Locate every Plasmodium falciparum-infected red blood cell.
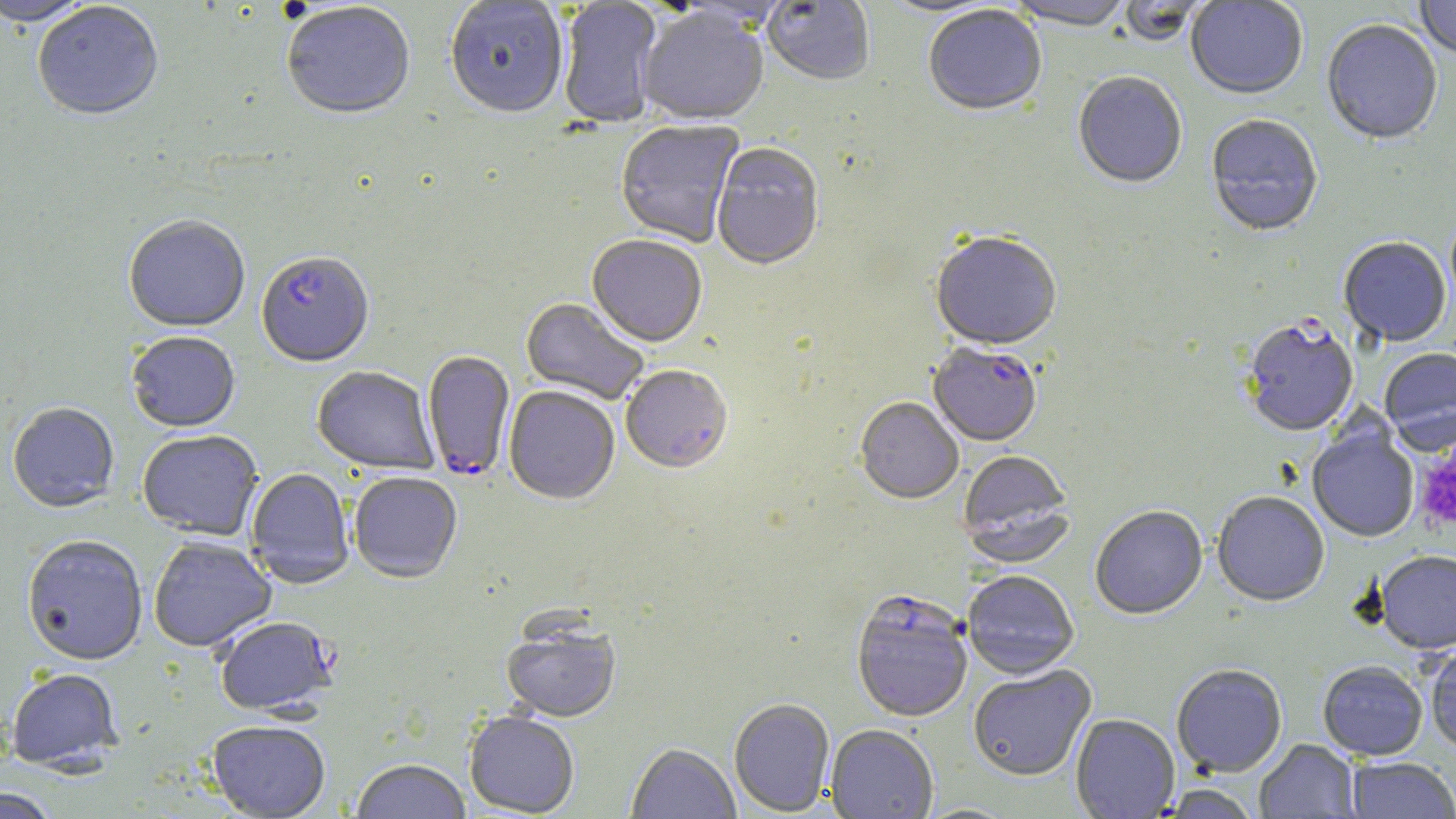

Approximate bounding boxes as [x1, y1, x2, y2] in pixels.
Plasmodium falciparum-infected red blood cells: [257, 254, 374, 369], [1242, 321, 1359, 438], [928, 345, 1042, 449], [422, 351, 515, 482], [851, 592, 973, 724], [214, 617, 338, 718].

Platelet locations: [1414, 449, 1456, 532]. Uninfected red blood cell locations: [762, 0, 875, 88], [877, 0, 1005, 18], [1186, 0, 1308, 101], [1414, 0, 1456, 60], [0, 1, 93, 28], [444, 1, 568, 122], [557, 1, 664, 130], [1007, 1, 1133, 34], [1117, 1, 1210, 48], [33, 3, 163, 124], [281, 4, 415, 123], [923, 6, 1047, 118], [637, 9, 769, 128], [1321, 21, 1442, 147], [1072, 74, 1187, 191], [1205, 115, 1323, 239], [615, 121, 745, 248], [711, 144, 824, 273], [123, 217, 250, 334], [930, 234, 1062, 352], [587, 237, 707, 350], [1339, 239, 1451, 348], [520, 299, 648, 405], [126, 333, 240, 434], [1379, 349, 1456, 454], [312, 367, 440, 475], [621, 367, 733, 477], [503, 387, 620, 506], [855, 399, 963, 506], [7, 403, 120, 514], [1307, 428, 1419, 543], [137, 431, 263, 541], [957, 453, 1075, 567], [246, 469, 354, 590], [349, 473, 462, 584], [1211, 493, 1329, 609], [1090, 507, 1208, 621], [21, 536, 148, 667], [149, 537, 276, 654], [1375, 553, 1456, 656], [962, 571, 1079, 681], [501, 622, 620, 723], [1425, 646, 1456, 754], [1318, 663, 1427, 761], [968, 666, 1096, 782], [1171, 666, 1287, 779], [6, 668, 123, 773], [729, 699, 835, 816], [464, 712, 579, 817], [1071, 715, 1179, 818], [207, 722, 331, 818], [826, 726, 938, 819], [1254, 740, 1360, 818], [627, 744, 740, 818], [1346, 758, 1456, 819], [351, 760, 471, 819], [1158, 785, 1260, 819], [0, 789, 59, 818]. Slide-level diagnosis: Plasmodium falciparum. Thin blood smear. 1000x magnification. Image is 1456×819 pixels. Optical microscopy. May-Grünwald-Giemsa-stained preparation. Single field of view.